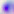
Summary:
  - Identification: Toxoplasma gondii
  - Modality: photomicrograph
  - Magnification: 400x